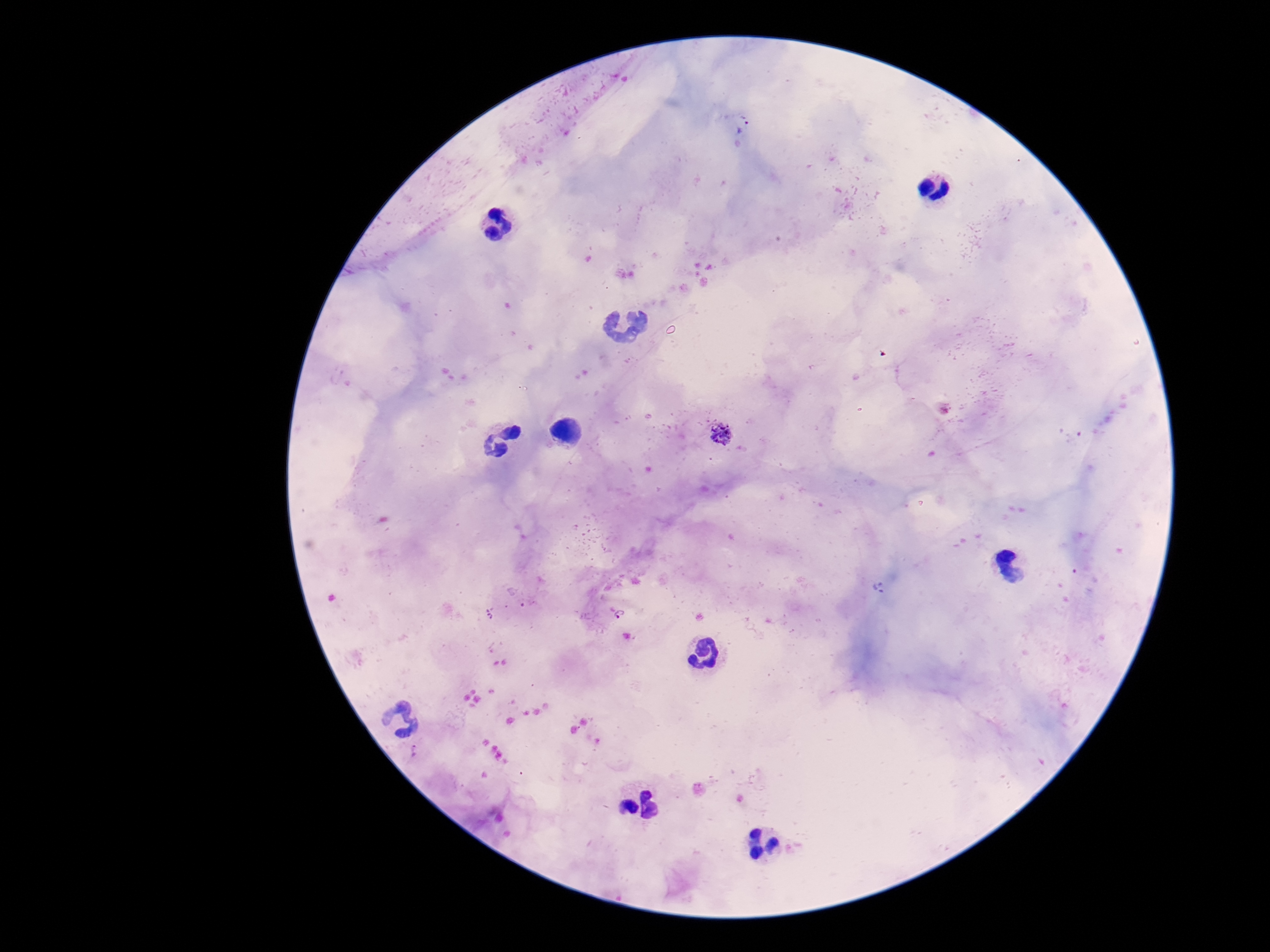

capture = smartphone camera through the microscope eyepiece
patient malaria status = positive
preparation = thick blood film
Plasmodium parasite locations = approximate centers as [x, y] in pixels: [743, 124], [723, 434], [621, 615], [415, 750]
magnification = 100x
stain = Giemsa
field of view = single
image size = 1270×952 pixels